Name the parasite shown.
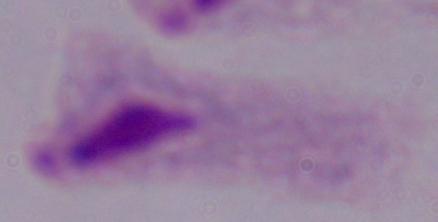
A trichomonad.

Captured at 1000x magnification. Photomicrograph.